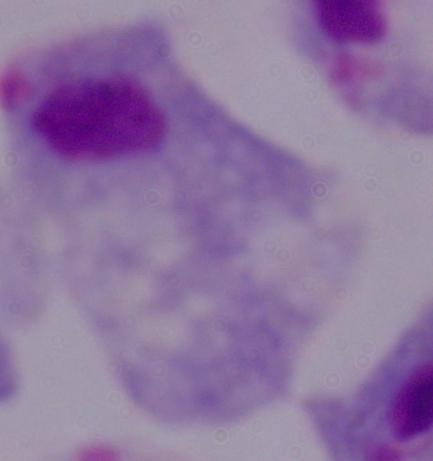
Summary:
  - Identification: trichomonad
  - Magnification: 1000x
  - Modality: photomicrograph